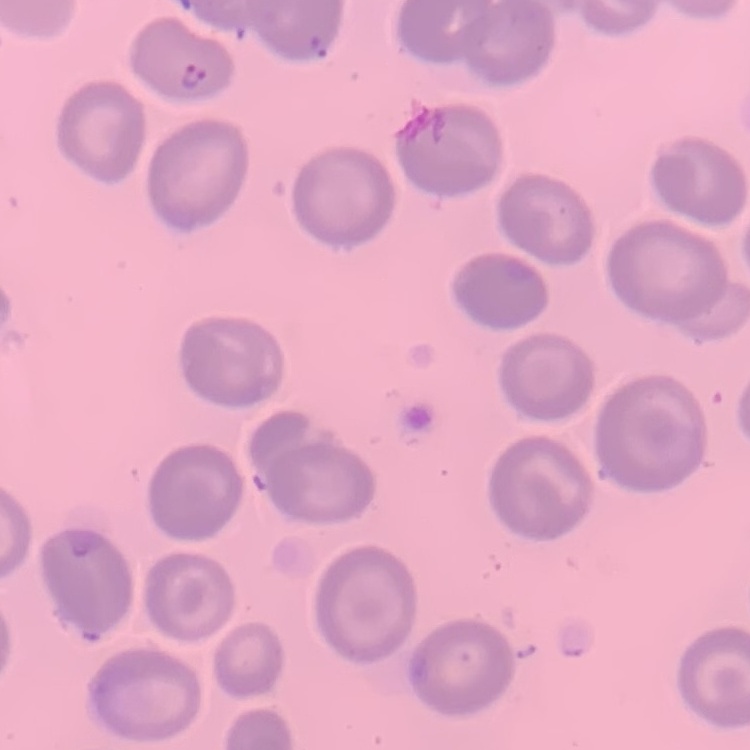

The erythrocytes show no rouleaux formation. One tile cut from a larger photomicrograph. Stained with either Field's or Giemsa. Thin blood smear.